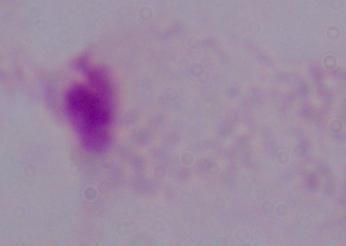
Summary:
  - Modality: micrograph
  - Identification: trichomonad
  - Magnification: 1000x